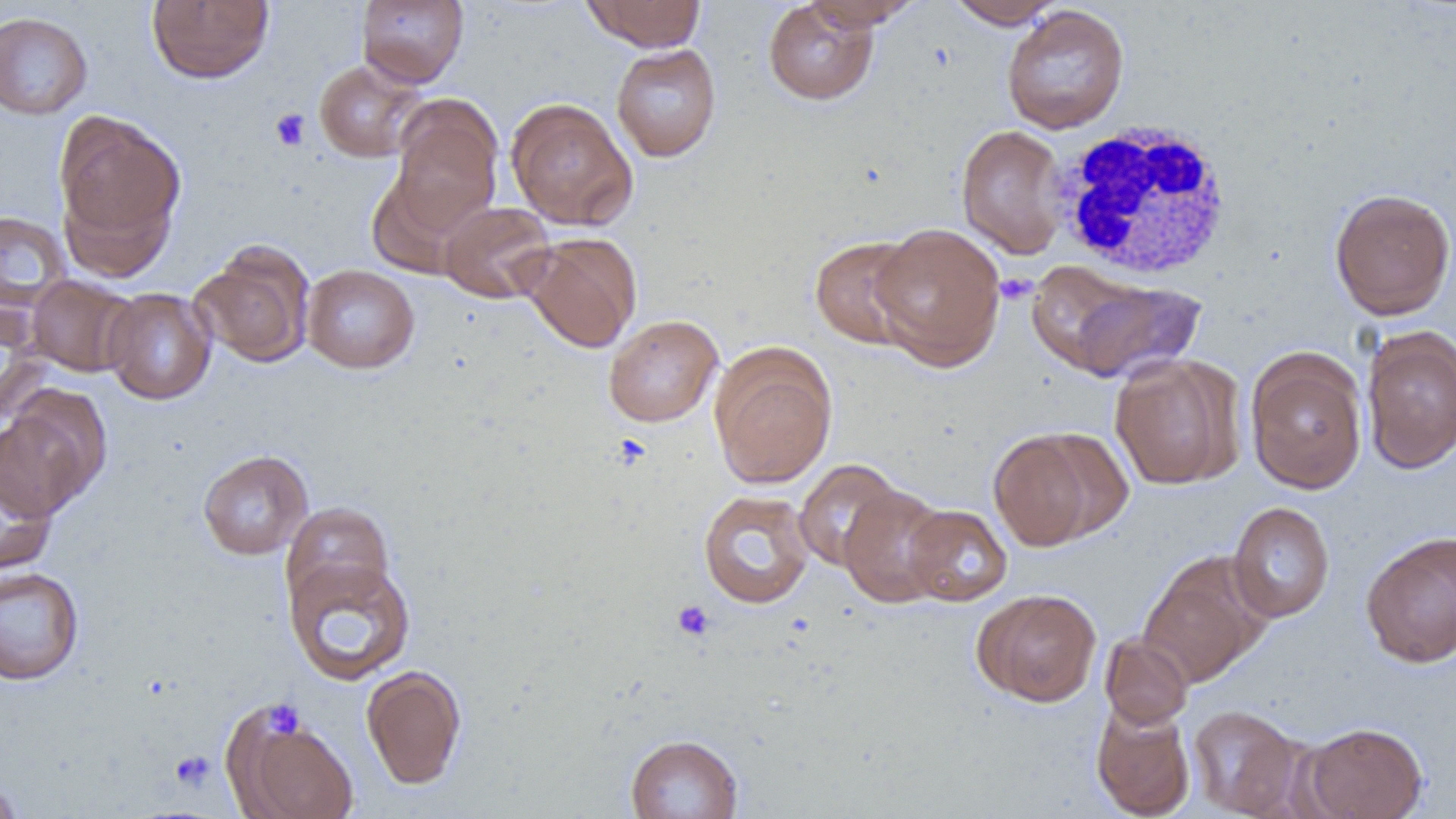

Summary:
  - Coordinate format: approximate bounding boxes as (x1, y1, x2, y2) in pixels
  - Platelet locations: (269, 108, 311, 151), (995, 273, 1038, 305), (672, 600, 715, 642), (263, 699, 305, 740), (169, 750, 216, 791)
  - Uninfected red blood cell locations: (146, 0, 275, 84), (356, 0, 469, 88), (582, 0, 707, 51), (763, 0, 880, 106), (944, 0, 1065, 29), (800, 1, 922, 30), (1001, 4, 1130, 135), (0, 11, 93, 120), (610, 43, 722, 162), (313, 60, 427, 163), (389, 96, 503, 235), (505, 97, 638, 231), (53, 111, 186, 260), (955, 124, 1069, 259), (1329, 187, 1456, 320), (439, 201, 556, 304), (0, 211, 71, 310), (868, 222, 1006, 370), (520, 232, 642, 353), (809, 234, 924, 350), (190, 244, 316, 368), (302, 264, 419, 374), (1036, 267, 1206, 383), (26, 274, 138, 377), (102, 287, 217, 405), (0, 300, 49, 423), (603, 314, 723, 428), (1360, 326, 1456, 474), (710, 346, 837, 489), (1245, 350, 1368, 494), (1109, 355, 1243, 490), (0, 397, 105, 517), (989, 428, 1109, 552), (197, 449, 313, 560), (0, 456, 59, 576), (793, 459, 906, 572), (839, 484, 951, 608), (697, 490, 816, 609), (1227, 501, 1335, 623), (281, 502, 395, 611), (904, 504, 1012, 607), (1360, 530, 1456, 668), (283, 556, 416, 686), (1138, 557, 1267, 689), (0, 566, 85, 685), (972, 588, 1102, 707), (1099, 633, 1194, 729), (361, 664, 467, 790), (224, 702, 361, 819), (1090, 702, 1196, 818), (1187, 704, 1306, 817), (1299, 721, 1428, 819), (625, 733, 744, 818), (0, 775, 25, 818)
  - White blood cell locations: (1048, 121, 1236, 281)
  - Slide-level diagnosis: negative for blood parasites
  - Field of view: single
  - Image size: 1456×819 pixels
  - Preparation: thin blood film
  - Modality: light microscopy
  - Magnification: 1000x